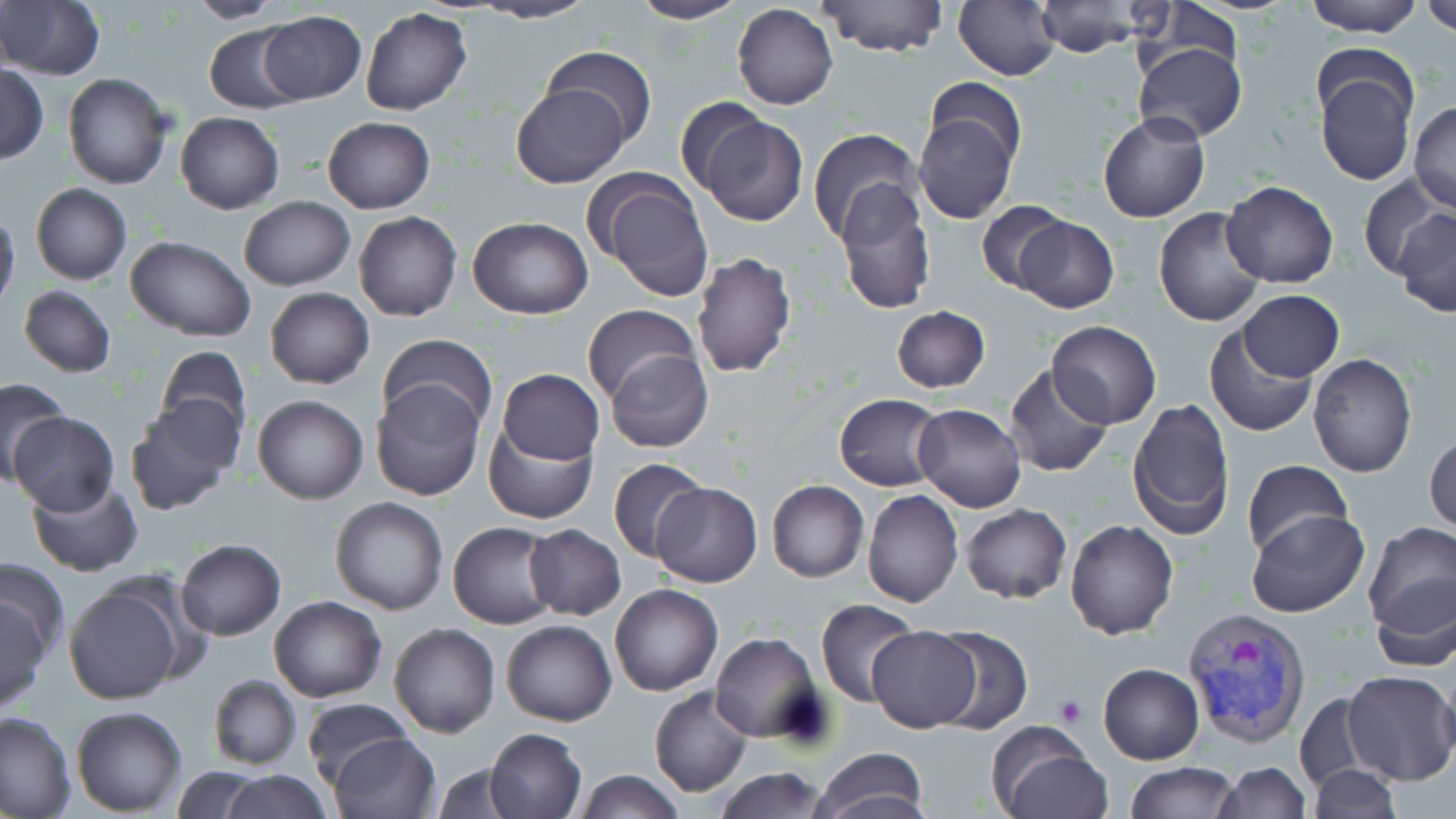

slide_level_diagnosis: Plasmodium vivax
modality: optical microscopy
stain: May-Grünwald-Giemsa
magnification: 1000x
image_size: 1456×819 pixels
field_of_view: one of a larger specimen
uninfected_red_blood_cell_locations: 'approximate bounding boxes as (x1,y1)-(x2,y2) corner pairs in pixels: (184,0)-(283,24), (629,0)-(750,24), (816,0)-(949,58), (953,0)-(1062,82), (1304,0)-(1421,37), (1421,0)-(1455,36), (472,1)-(600,24), (0,2)-(104,80), (730,4)-(838,111), (1034,4)-(1151,56), (360,7)-(473,116), (259,10)-(366,105), (206,24)-(304,114), (1133,41)-(1248,142), (541,45)-(657,144), (1312,58)-(1418,186), (1,63)-(47,162), (63,73)-(171,190), (924,73)-(1026,175), (510,83)-(628,188), (673,97)-(772,199), (1408,101)-(1456,214), (913,107)-(1020,224), (693,110)-(808,226), (1097,110)-(1210,223), (174,112)-(284,213), (323,117)-(435,213), (807,128)-(923,244), (590,172)-(713,302), (1358,175)-(1447,281), (1221,179)-(1339,288), (30,183)-(131,285), (834,185)-(937,316), (238,196)-(354,292), (975,201)-(1070,294), (0,207)-(20,316), (1154,208)-(1268,328), (1394,209)-(1456,319), (354,211)-(462,322), (467,216)-(593,319), (1013,216)-(1119,312), (124,236)-(256,342), (691,251)-(797,379), (19,286)-(115,377), (266,288)-(374,390), (1239,291)-(1343,380), (583,305)-(700,406), (891,306)-(989,393), (1046,321)-(1162,430), (1203,324)-(1320,437), (378,334)-(497,436), (154,344)-(250,444), (604,348)-(713,454), (1307,353)-(1417,477), (1004,365)-(1114,478), (497,368)-(603,466), (0,377)-(71,479), (370,382)-(485,501), (833,394)-(946,491), (252,395)-(368,504), (1127,397)-(1236,539), (124,399)-(241,515), (914,404)-(1026,513), (9,410)-(120,514), (485,426)-(597,523), (1426,432)-(1456,536), (607,457)-(710,565), (1242,459)-(1352,559), (25,475)-(143,577), (767,480)-(869,583), (649,482)-(761,586), (862,489)-(965,608), (330,497)-(448,615), (961,504)-(1071,603), (1246,510)-(1369,618), (1066,519)-(1179,639), (448,521)-(559,630), (1361,522)-(1456,639), (524,525)-(626,620), (175,538)-(286,641), (0,558)-(69,667), (1369,573)-(1456,673), (62,577)-(191,706), (609,584)-(722,696), (0,591)-(51,717), (269,595)-(387,703), (815,601)-(922,707), (501,619)-(616,726), (389,622)-(499,737), (866,625)-(981,731), (927,626)-(1033,736), (712,632)-(824,743), (1098,663)-(1204,765), (1342,672)-(1456,786), (208,674)-(300,770), (649,687)-(752,798), (1294,691)-(1379,796), (302,697)-(415,788), (71,706)-(188,816), (0,710)-(75,817), (986,724)-(1108,819), (483,726)-(587,819), (328,731)-(440,818), (809,748)-(929,819), (1122,760)-(1240,818), (1216,762)-(1309,818), (432,763)-(528,818), (1306,764)-(1403,819), (170,766)-(267,819), (712,767)-(831,819), (220,770)-(333,818), (575,770)-(687,818)'
preparation: thin blood film
platelet_locations: 'approximate bounding boxes as (x1,y1)-(x2,y2) corner pairs in pixels: (1053,694)-(1087,727)'
plasmodium_vivax_infected_red_blood_cell_locations: 'approximate bounding boxes as (x1,y1)-(x2,y2) corner pairs in pixels: (1182,607)-(1312,749)'